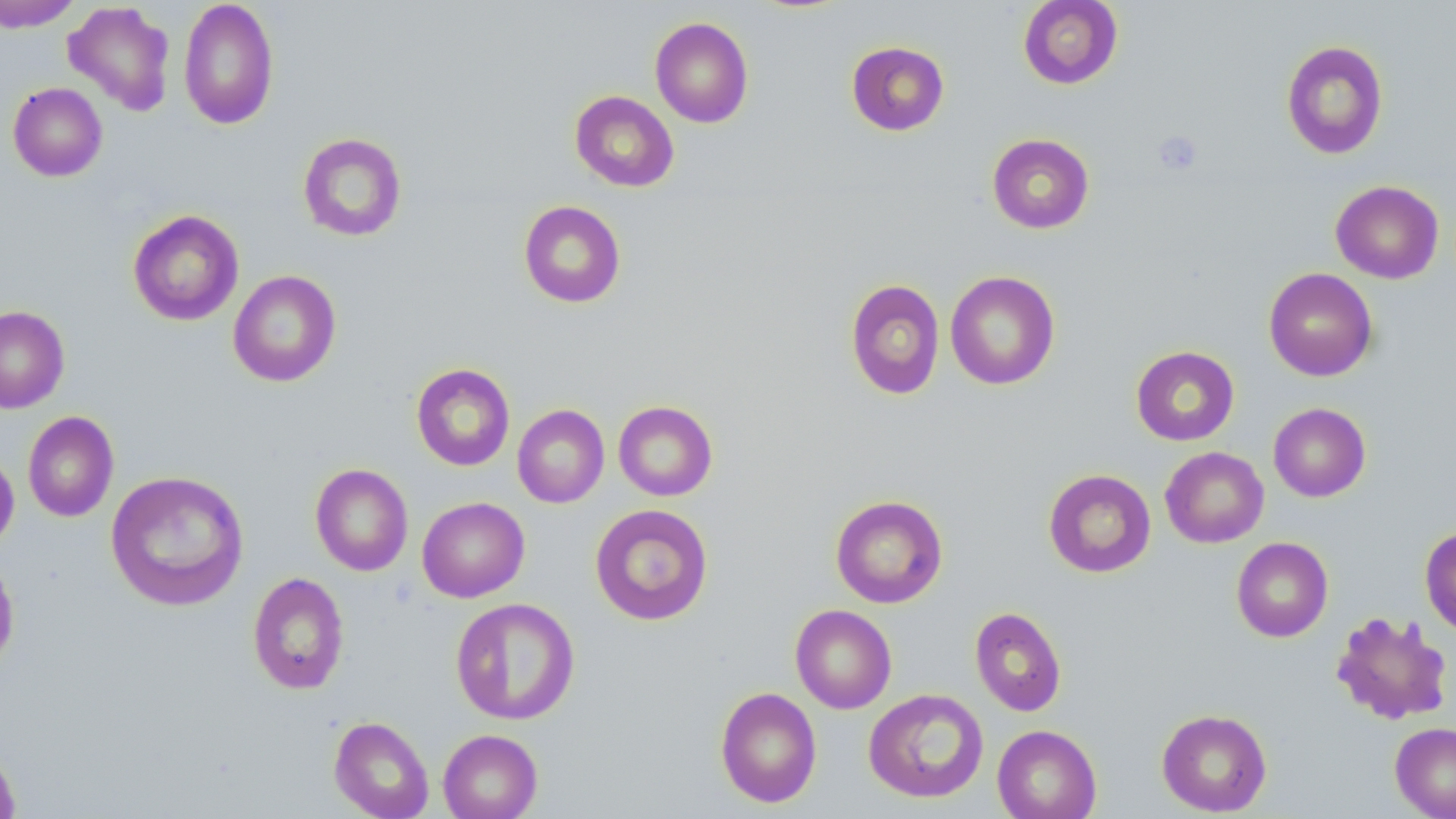
slide-level diagnosis = no evidence of blood parasites
preparation = thin blood film
stain = May-Grünwald-Giemsa
magnification = 1000x
field of view = single
modality = optical microscopy
platelet locations = approximate bounding boxes as (x1, y1, x2, y2) in pixels: (1152, 130, 1203, 176)
uninfected red blood cell locations = approximate bounding boxes as (x1, y1, x2, y2) in pixels: (178, 0, 279, 130), (1017, 0, 1123, 89), (0, 1, 83, 32), (63, 1, 177, 116), (650, 17, 754, 128), (845, 40, 950, 136), (1280, 40, 1389, 160), (8, 82, 108, 181), (569, 90, 679, 192), (297, 132, 407, 242), (986, 133, 1095, 234), (1330, 180, 1445, 284), (518, 200, 626, 308), (127, 209, 244, 326), (1263, 267, 1378, 381), (227, 269, 341, 388), (945, 270, 1060, 390), (845, 279, 945, 400), (0, 305, 70, 413), (1130, 345, 1240, 446), (411, 363, 515, 471), (613, 400, 718, 501), (1268, 403, 1371, 502), (512, 404, 609, 508), (23, 411, 119, 522), (0, 447, 19, 553), (1160, 447, 1269, 548), (310, 463, 413, 576), (1043, 468, 1156, 578), (105, 470, 249, 611), (830, 494, 948, 608), (417, 497, 530, 602), (589, 503, 713, 626), (1419, 526, 1456, 636), (1231, 537, 1333, 642), (0, 551, 19, 673), (247, 572, 349, 695), (450, 597, 581, 725), (790, 604, 897, 714), (969, 606, 1067, 717), (1330, 610, 1454, 726), (715, 686, 822, 808), (863, 688, 989, 803), (1156, 709, 1272, 816), (329, 716, 434, 819), (1390, 722, 1456, 819), (992, 724, 1102, 819), (438, 728, 543, 819), (0, 741, 20, 819)
image size = 1456×819 pixels